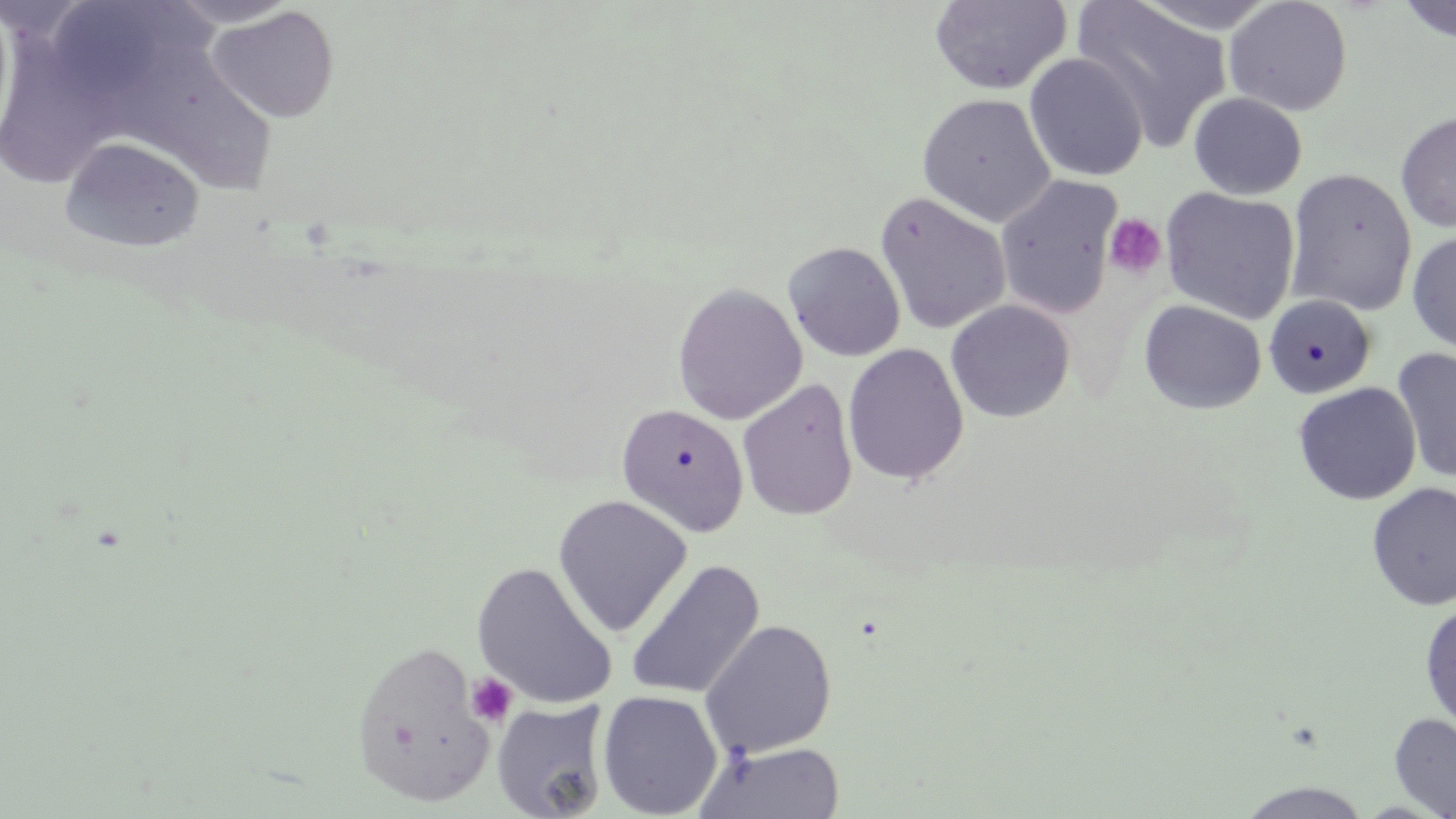
Summary:
  - Coordinate format: approximate bounding boxes as (x1,y1)-(x2,y2) corner pairs in pixels
  - Platelet locations: (1104,214)-(1167,279), (465,673)-(517,727)
  - Uninfected red blood cell locations: (163,0)-(301,29), (1072,0)-(1232,150), (1224,0)-(1353,116), (1396,0)-(1456,43), (929,1)-(1071,94), (207,5)-(340,124), (0,23)-(119,189), (1024,53)-(1148,183), (1188,92)-(1308,200), (916,93)-(1056,227), (1395,111)-(1456,232), (59,136)-(206,253), (1285,168)-(1417,316), (995,175)-(1123,321), (1160,188)-(1300,326), (874,191)-(1012,335), (1407,230)-(1456,354), (783,241)-(906,362), (672,282)-(807,425), (1263,294)-(1377,400), (946,299)-(1075,423), (1139,299)-(1266,414), (843,343)-(969,485), (1392,346)-(1455,484), (737,379)-(858,522), (1292,382)-(1422,506), (614,402)-(750,538), (1366,482)-(1456,611), (551,494)-(694,637), (625,559)-(765,701), (472,561)-(618,709), (1420,600)-(1456,733), (700,620)-(837,757), (349,639)-(496,806), (597,690)-(723,818), (491,699)-(610,818), (1389,712)-(1456,819), (692,740)-(847,819), (1234,781)-(1375,819)
  - Slide-level diagnosis: negative for blood parasites
  - Preparation: thin blood film
  - Field of view: one of a larger specimen
  - Modality: optical microscopy
  - Stain: May-Grünwald-Giemsa
  - Image size: 1456×819 pixels
  - Magnification: 1000x